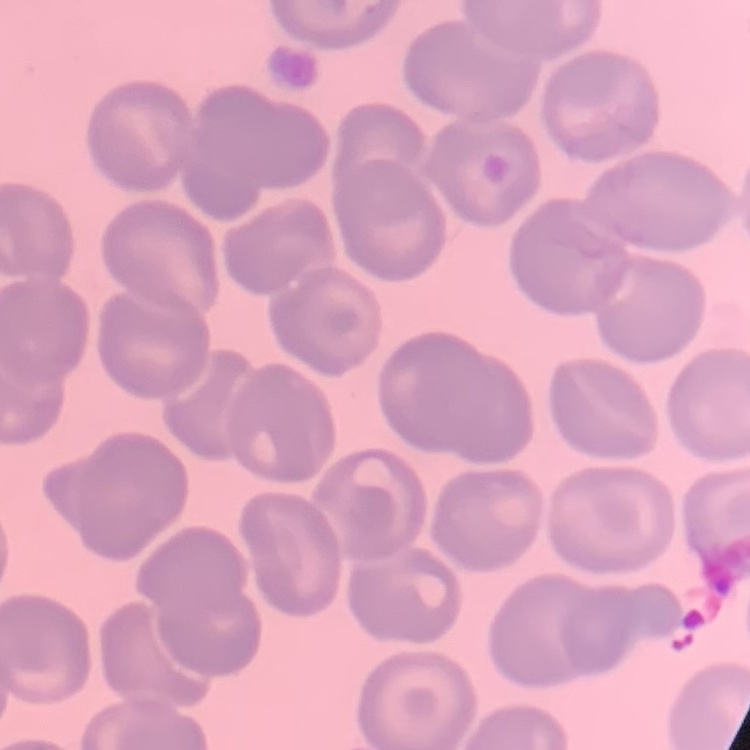

red blood cell morphology = no rouleaux formation
image type = one tile cut from a larger photomicrograph
preparation = thin blood smear
stain = Field's or Giemsa